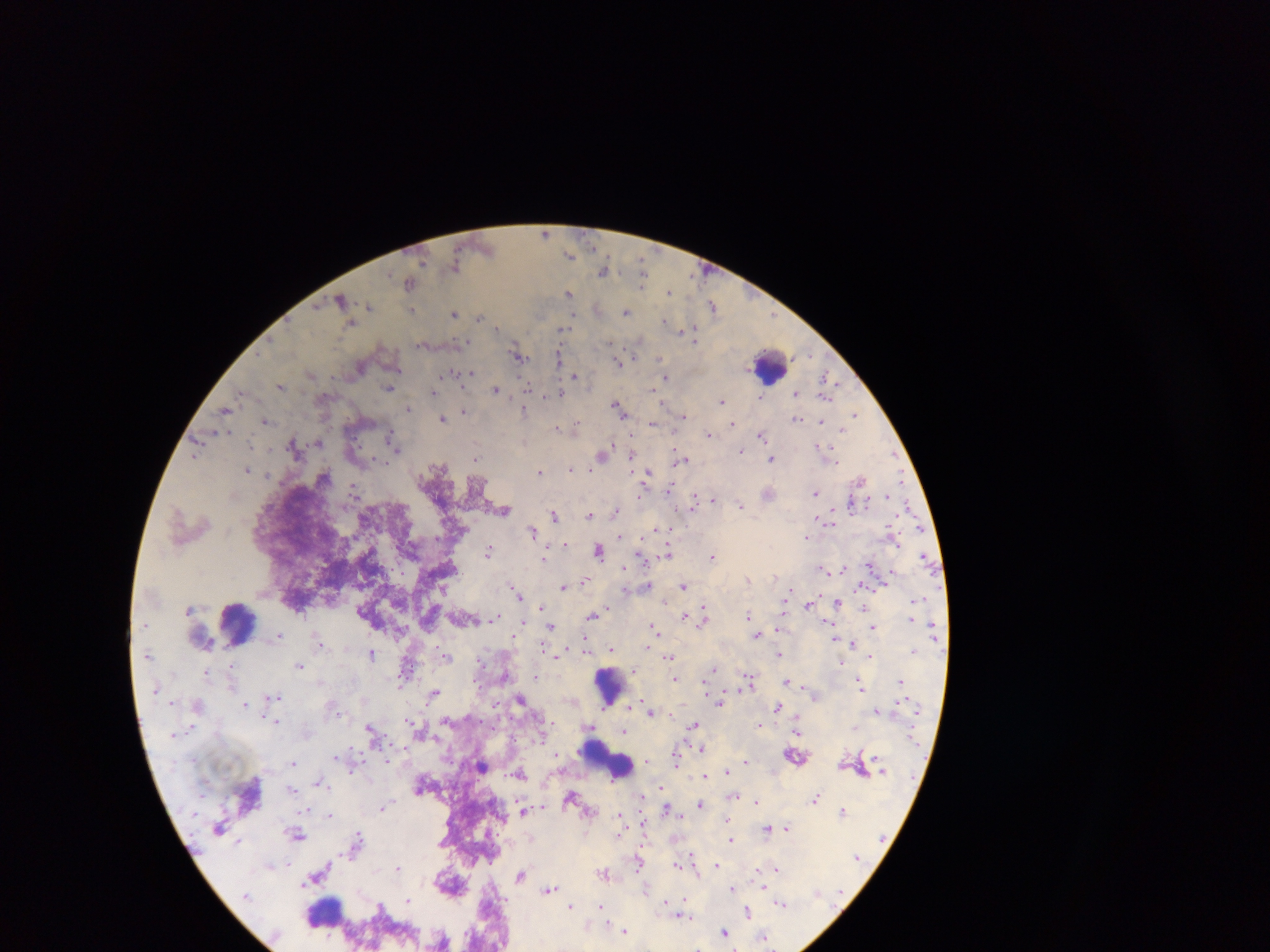

{
  "preparation": "thick blood film",
  "capture": "mobile-phone photograph through a microscope",
  "country": "Ghana",
  "image_size": "1270×952 pixels",
  "field_of_view": "single",
  "malaria_parasite_locations": "approximate centers as (x, y) in pixels: (545, 232), (570, 254), (455, 266), (643, 268), (603, 271), (643, 275), (410, 283), (642, 284), (668, 292), (569, 293), (342, 298), (370, 306), (713, 306), (412, 310), (627, 311), (454, 313), (479, 318), (666, 321), (496, 326), (563, 329), (681, 330), (691, 334), (694, 339), (518, 355), (559, 357), (661, 358), (618, 362), (453, 373), (472, 373), (575, 375), (666, 377), (828, 379), (280, 386), (389, 388), (529, 389), (497, 390), (434, 391), (241, 393), (794, 393), (560, 394), (760, 397), (722, 400), (618, 407), (407, 408), (226, 410), (464, 411), (524, 411), (856, 414), (683, 416), (442, 418), (798, 419), (265, 420), (822, 422), (652, 423), (731, 424), (577, 426), (556, 427), (708, 433), (761, 434), (199, 441), (393, 441), (318, 443), (397, 449), (740, 450), (827, 452), (603, 454), (194, 456), (476, 457), (632, 457), (831, 457), (682, 459), (770, 459), (570, 469), (247, 470), (540, 471), (646, 476), (860, 480), (355, 489), (669, 489), (769, 493), (816, 493), (887, 495), (713, 499), (694, 502), (851, 504), (740, 505), (504, 511), (616, 511), (554, 515), (588, 515), (829, 522), (533, 531), (806, 537), (563, 544), (668, 549), (599, 550), (490, 551), (544, 557), (712, 557), (870, 564), (844, 567), (823, 569), (584, 581), (648, 586), (683, 586), (564, 587), (518, 594), (838, 602), (808, 604), (541, 608), (864, 608), (593, 616), (684, 616), (748, 616), (497, 617), (704, 617), (912, 618), (828, 625), (551, 626), (873, 626), (654, 629), (280, 635), (758, 635), (834, 638), (319, 642), (852, 644), (611, 649), (372, 654), (779, 655), (871, 656), (447, 657), (669, 658), (841, 663), (299, 666), (406, 668), (713, 670), (206, 672), (536, 677), (674, 679), (750, 680), (788, 681), (900, 681), (861, 685), (434, 693), (274, 697), (521, 700), (720, 702), (198, 704), (246, 704), (778, 708), (877, 710), (650, 711), (274, 720), (413, 723), (760, 724), (693, 726), (855, 727), (371, 731), (624, 732), (701, 749), (557, 755), (796, 755), (676, 759), (646, 761), (745, 761), (293, 762), (482, 766), (727, 771), (519, 774), (704, 776), (321, 783), (419, 786), (292, 790), (733, 796), (570, 798), (815, 798), (757, 802), (701, 804), (383, 806), (668, 809), (842, 810), (523, 811), (331, 816), (620, 817), (727, 821), (787, 827), (767, 828), (297, 834), (731, 839), (356, 842), (691, 857), (639, 864), (716, 865), (398, 868), (776, 868), (605, 872), (520, 875), (549, 889), (732, 889), (408, 900), (782, 904), (380, 906), (571, 906), (600, 907), (748, 912), (683, 915), (625, 930), (724, 931), (764, 936)",
  "leukocyte_locations": "approximate centers as (x, y) in pixels (subset; some below the resolvable size): (771, 366), (238, 626), (612, 689), (608, 758), (324, 911)"
}